Report the malaria status of this cell.
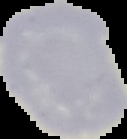
Uninfected.

image type = segmented cell region with the area outside set to black
preparation = thin blood smear
image size = 127×139 pixels